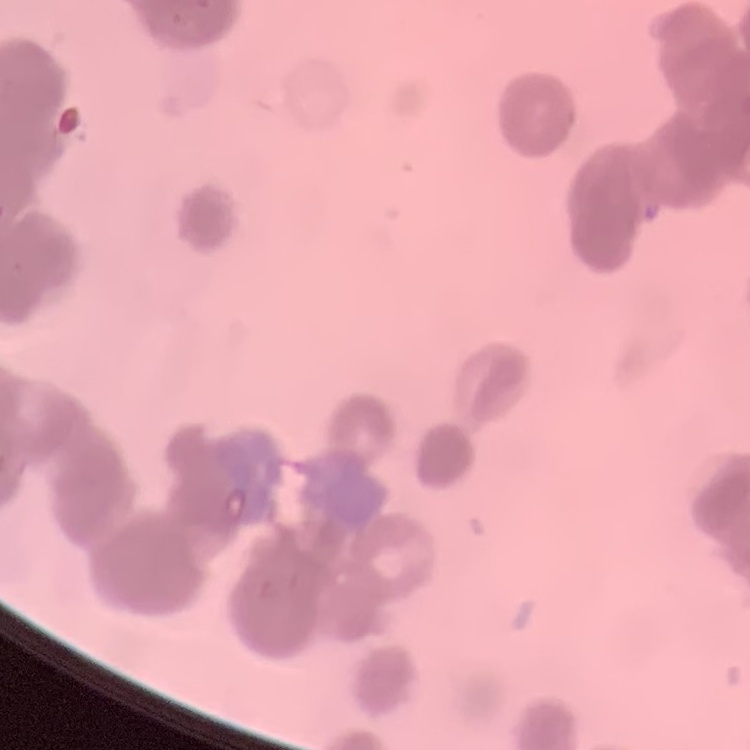

red_blood_cell_morphology: rouleaux formation
preparation: thin peripheral smear
image_type: one tile cut from a larger photomicrograph
stain: Field's or Giemsa